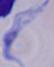
Summary:
  - Identification: trypanosome
  - Magnification: 1000x
  - Modality: micrograph